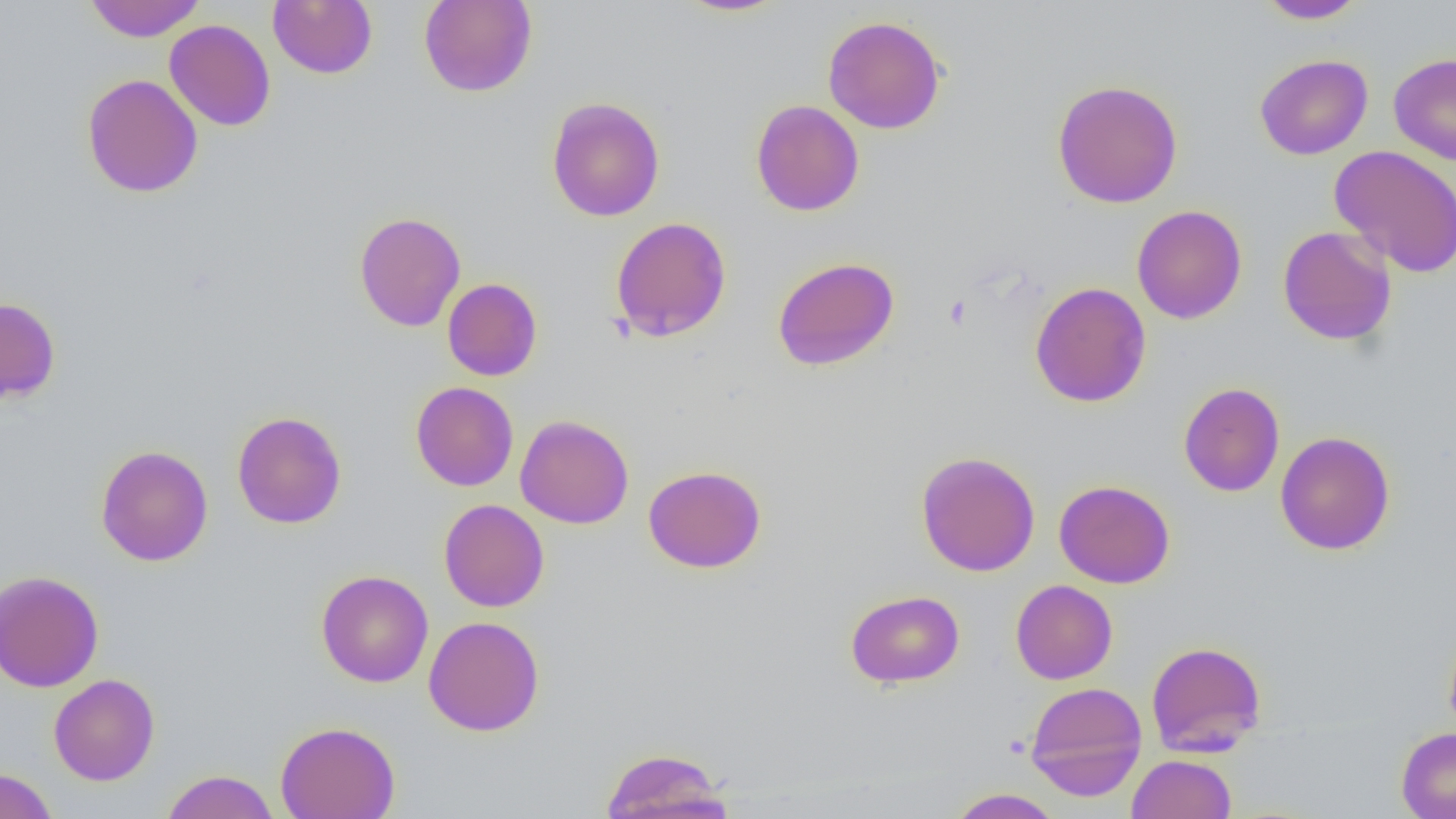

Summary:
  - Coordinate format: approximate bounding boxes as (x1, y1, x2, y2) in pixels
  - Platelet locations: (943, 295, 971, 330)
  - Uninfected red blood cell locations: (83, 0, 206, 42), (418, 0, 537, 97), (674, 0, 791, 17), (1256, 0, 1368, 24), (268, 1, 378, 79), (822, 15, 946, 134), (164, 19, 276, 131), (1388, 53, 1456, 165), (1254, 54, 1373, 160), (82, 73, 203, 198), (1051, 79, 1184, 208), (546, 96, 665, 222), (751, 100, 864, 216), (1329, 144, 1456, 278), (1131, 205, 1247, 324), (354, 211, 466, 332), (609, 216, 732, 342), (1277, 226, 1397, 346), (772, 256, 899, 371), (442, 278, 542, 381), (1030, 281, 1151, 407), (0, 296, 61, 405), (410, 381, 519, 491), (1178, 381, 1285, 497), (232, 411, 346, 529), (515, 414, 634, 529), (1275, 430, 1395, 556), (95, 444, 213, 567), (915, 451, 1041, 577), (643, 465, 766, 573), (1054, 479, 1175, 588), (439, 499, 549, 612), (0, 570, 104, 693), (316, 570, 433, 687), (1010, 580, 1118, 684), (845, 589, 964, 688), (423, 615, 545, 736), (1443, 624, 1456, 739), (1146, 640, 1267, 758), (48, 673, 160, 785), (1024, 681, 1147, 801), (275, 720, 400, 819), (1396, 727, 1456, 819), (599, 747, 733, 819), (1126, 754, 1236, 819), (0, 767, 58, 819), (160, 769, 279, 819), (946, 788, 1064, 818)
  - Slide-level diagnosis: no evidence of blood parasites
  - Magnification: 1000x
  - Preparation: thin blood film
  - Image size: 1456×819 pixels
  - Field of view: one of a larger specimen
  - Modality: optical microscopy